Name the parasite shown.
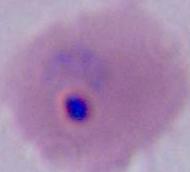

This is Plasmodium.

400x or 1000x magnification. Micrograph.